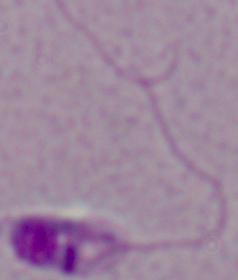
Summary:
  - Identification: Leishmania
  - Modality: micrograph
  - Magnification: 1000x